Name the parasite shown.
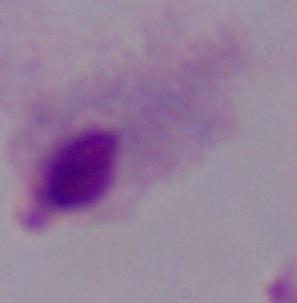

This is a trichomonad.

Summary:
  - Modality: micrograph
  - Magnification: 1000x